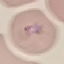
{
  "result": "malaria parasites detected",
  "stain": "Giemsa",
  "image_type": "cell patch, automatically extracted from a larger field of view and resized to 64 × 64 pixels",
  "preparation": "thin blood film",
  "capture": "smartphone camera at the microscope eyepiece"
}